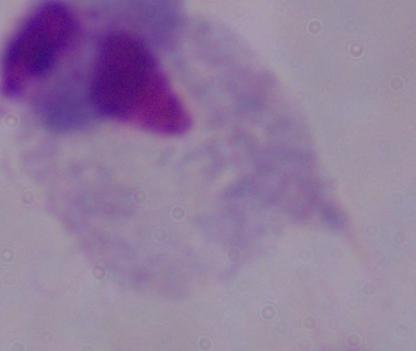 A trichomonad is seen. Photomicrograph. Captured at 1000x magnification.